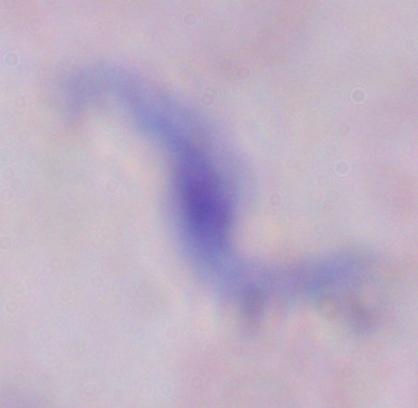

A trypanosome is seen. Micrograph. 1000x magnification.